Give the position of every malaria parasite.
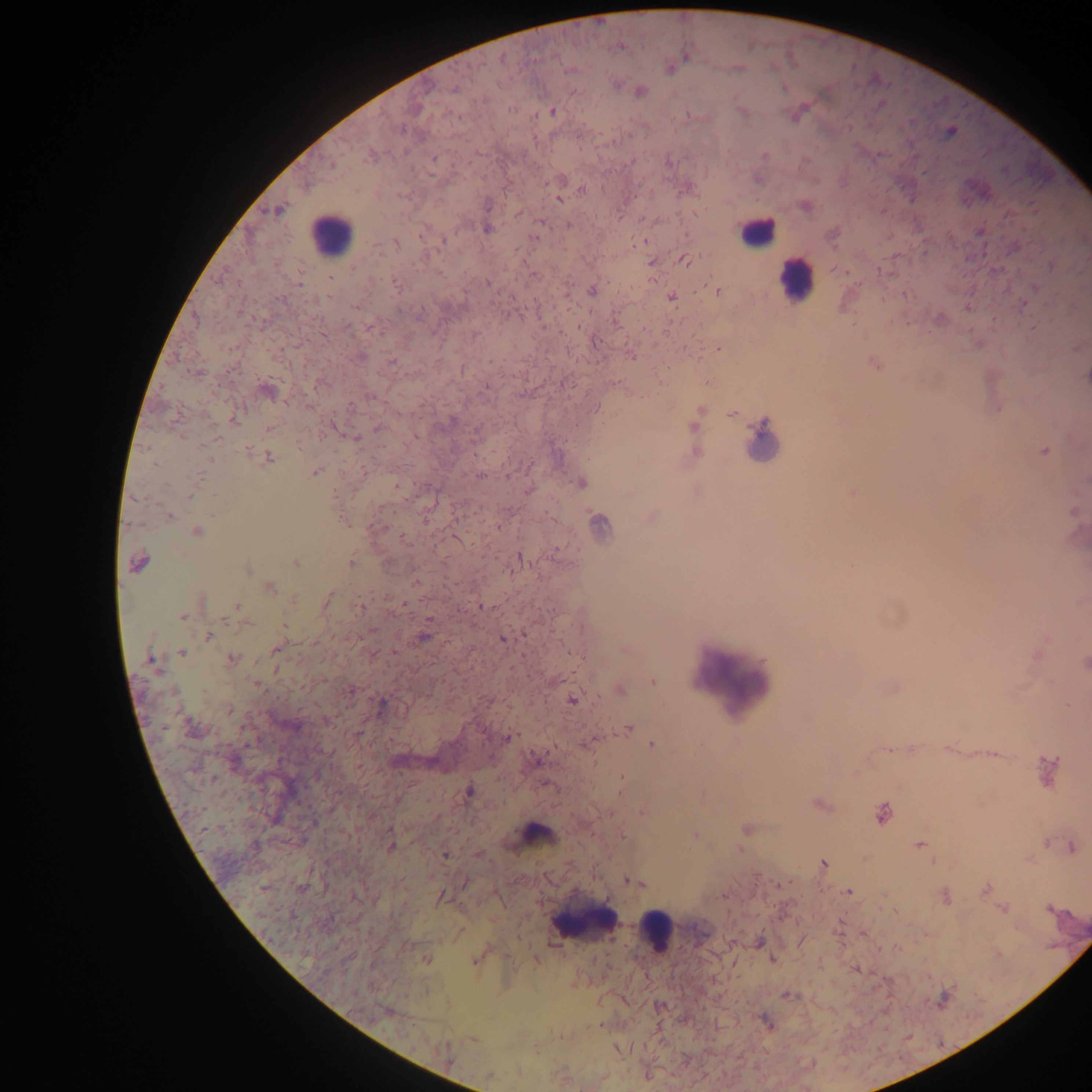
Approximate centers as x y in pixels.
Malaria parasites: 618 48; 686 57; 738 68; 641 91; 511 109; 552 111; 950 132; 434 157; 333 165; 581 190; 559 199; 488 205; 277 210; 541 222; 568 225; 487 229; 444 240; 640 241; 396 242; 684 260; 652 263; 353 267; 535 275; 330 279; 487 283; 299 284; 396 284; 1035 289; 592 291; 718 291; 671 297; 1024 304; 355 307; 196 320; 370 328; 324 335; 718 348; 361 356; 632 357; 391 361; 462 369; 486 387; 267 391; 372 397; 309 407; 596 408; 699 413; 732 414; 234 420; 694 426; 334 428; 377 428; 268 429; 217 438; 356 439; 298 446; 696 452; 1045 452; 268 458; 156 464; 316 472; 481 476; 508 476; 197 477; 580 483; 397 486; 853 493; 335 495; 1074 512; 169 516; 652 517; 343 520; 599 524; 377 527; 499 527; 196 532; 403 538; 520 558; 295 562; 138 563; 351 563; 248 570; 416 581; 269 587; 294 598; 326 602; 403 604; 237 606; 481 606; 360 608; 183 616; 284 625; 526 635; 209 636; 424 637; 503 639; 276 649; 182 653; 232 658; 151 661; 1085 664; 653 681; 256 684; 350 690; 620 690; 572 700; 382 704; 230 710; 291 726; 193 729; 628 729; 508 737; 653 745; 889 750; 538 760; 1048 770; 469 792; 821 804; 883 814; 747 828; 695 835; 920 845; 391 847; 1072 847; 445 854; 823 863; 635 881; 986 890; 849 892; 441 897; 946 897; 1003 909; 1048 909; 761 942; 427 959; 473 961; 856 970; 788 995; 766 1023; 471 1039; 618 1050.

leukocyte locations = approximate centers as x y in pixels: 756 233; 331 234; 795 280; 763 444; 735 679; 537 833; 586 922; 655 932
country = Ghana
image size = 1092×1092 pixels
capture = mobile-phone photograph through a microscope
preparation = thick blood film
field of view = single